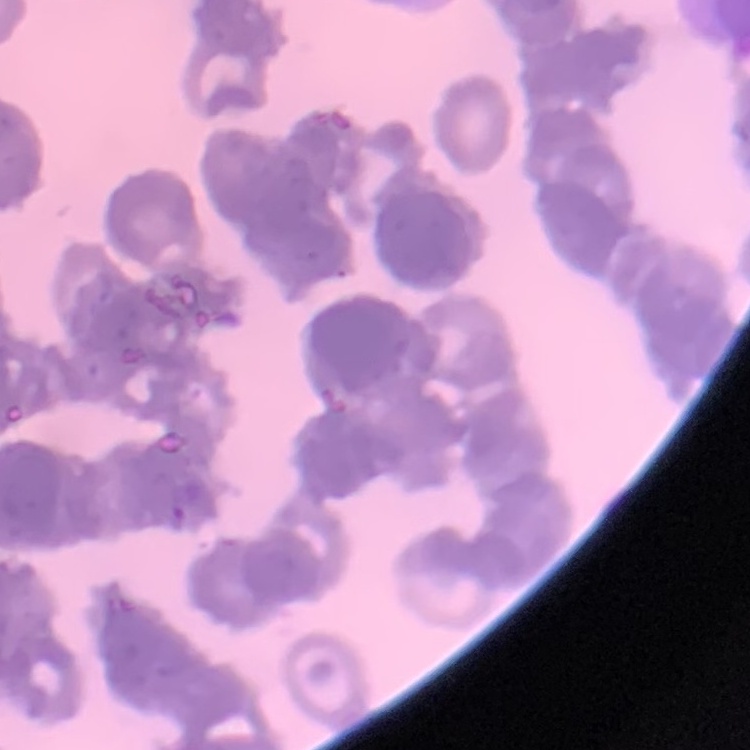
The erythrocytes show rouleaux formation. Thin blood smear. Square crop of a larger photomicrograph. Field's or Giemsa stain.